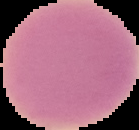
image size = 139×130 pixels
image type = segmented cell region with the area outside set to black
malaria status = uninfected
preparation = thin blood film